Report the malaria status of this cell.
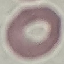
It is uninfected.

Cell patch, automatically extracted from a larger field of view and resized to 64 × 64 pixels. Giemsa-stained preparation. Acquired by smartphone through the microscope eyepiece. Thin blood smear.